State the preparation type.
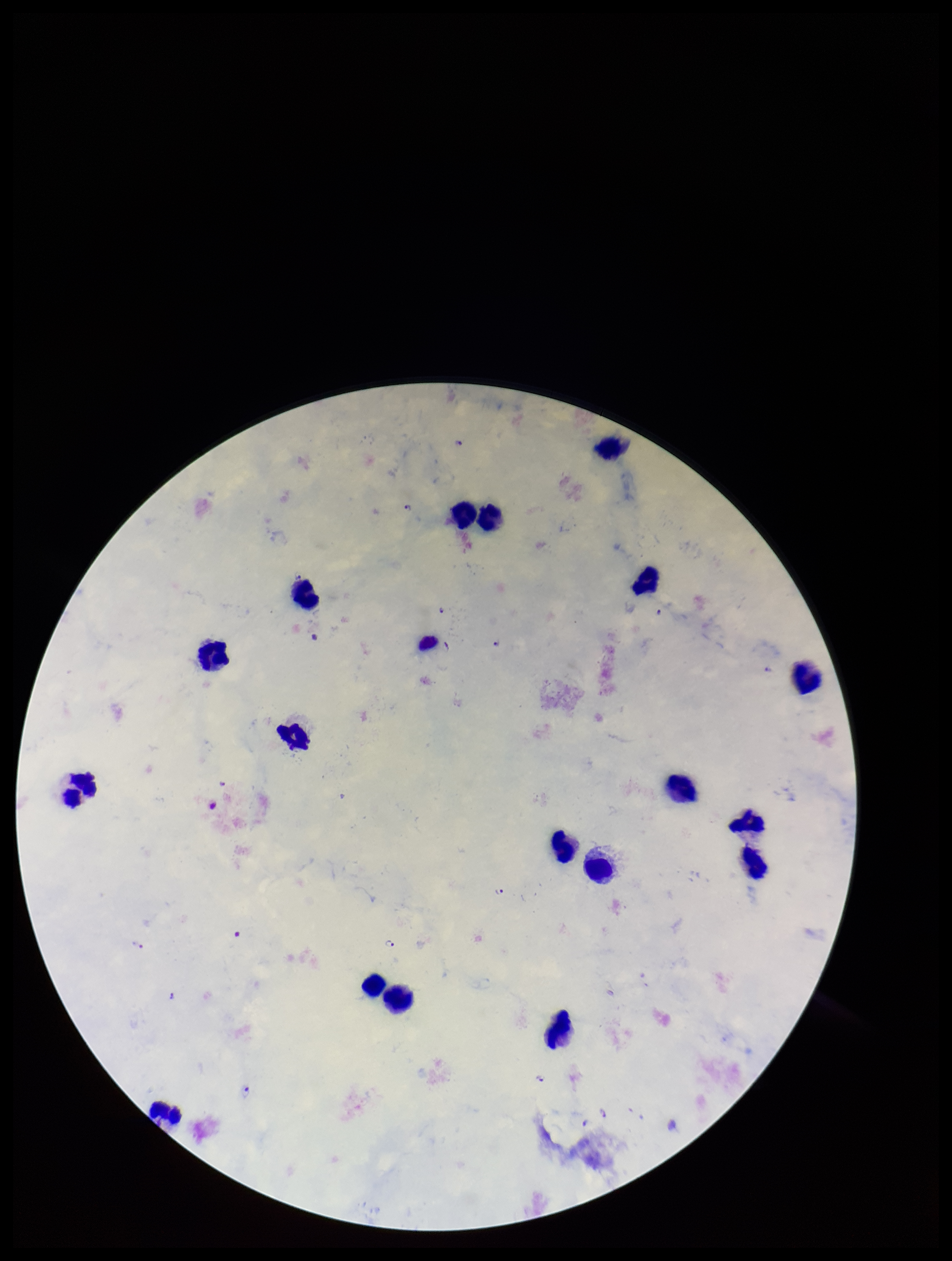
Thick.

Smartphone photograph taken through the eyepiece of a microscope. Single field of view. Leukocyte count: 18. Giemsa stain. Species reported for this patient: Plasmodium falciparum. Patient malaria status: positive. Image is 952×1261 pixels. Plasmodium parasites: identified. Parasite count: 11.